Report the malaria status of this cell.
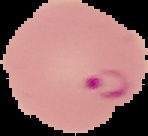
Parasitized.

From a thin blood film. Cell region segmented out of the field of view; the surrounding area is masked to black. Image is 148×136 pixels.